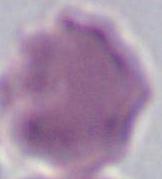

modality = photomicrograph
magnification = 1000x
identification = red blood cell